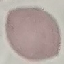

Summary:
  - Malaria status: uninfected
  - Image type: automatically extracted cell patch, resized to 64 × 64 pixels
  - Stain: Giemsa
  - Capture: smartphone camera at the microscope eyepiece
  - Preparation: thin blood smear